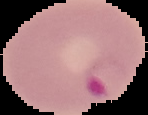

Summary:
  - Malaria status: parasitized
  - Image type: segmented cell region with the area outside set to black
  - Preparation: thin blood smear
  - Image size: 148×115 pixels